State which parasite is depicted.
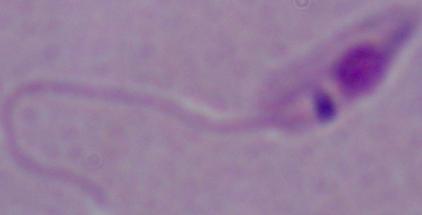
This is Leishmania.

Photomicrograph. 1000x magnification.